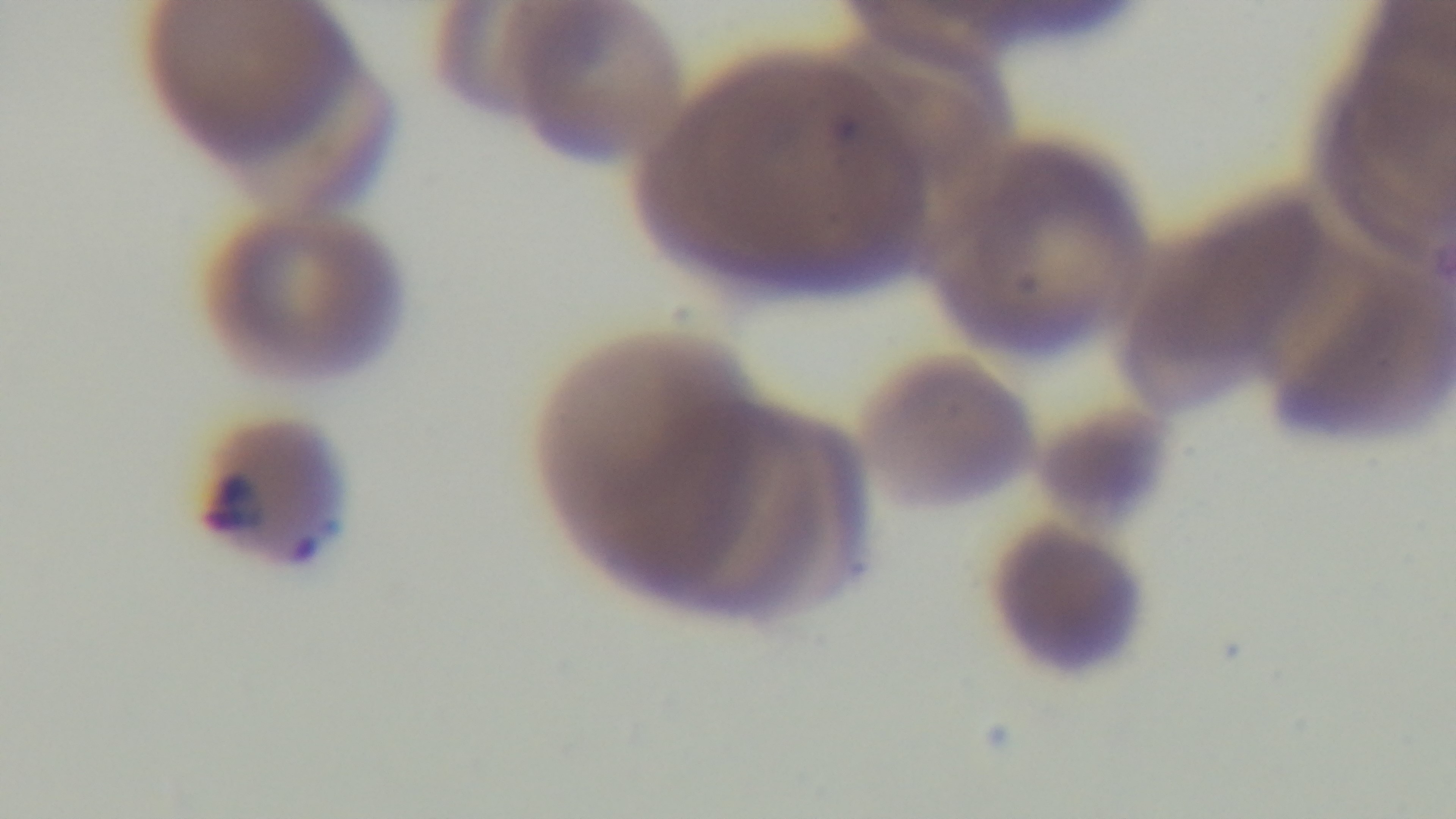

One field from the slide. Malaria status: positive. Light microscopy. Giemsa-stained. Captured with a mounted 4K digital camera. Preparation: thin smear. 100x oil-immersion objective.